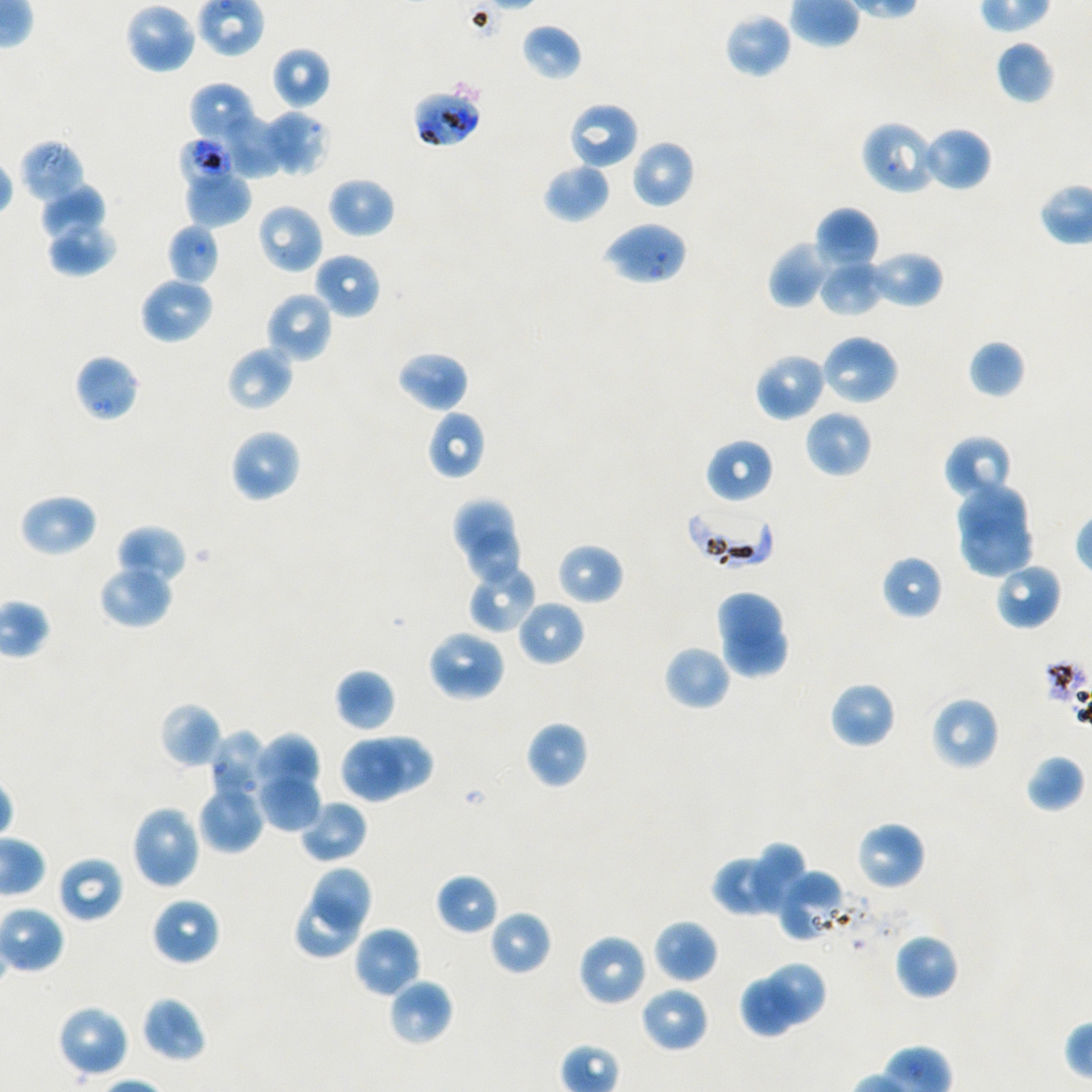

Not every red blood cell is marked. A life-cycle stage — or a range of stages, where the recorded stages span more than one — follows each staged infected red blood cell.
locations of uninfected red blood cells = approximate bounding rectangles given as corner coordinates in pixels from the top-left: (x1=124, y1=2, x2=197, y2=74), (x1=723, y1=12, x2=793, y2=78), (x1=521, y1=23, x2=583, y2=81), (x1=995, y1=40, x2=1055, y2=105), (x1=270, y1=46, x2=331, y2=110), (x1=189, y1=83, x2=260, y2=145), (x1=566, y1=101, x2=640, y2=170), (x1=261, y1=111, x2=331, y2=176), (x1=220, y1=117, x2=285, y2=179), (x1=921, y1=126, x2=992, y2=192), (x1=632, y1=140, x2=695, y2=209), (x1=543, y1=162, x2=611, y2=223), (x1=184, y1=167, x2=251, y2=226), (x1=327, y1=176, x2=396, y2=238), (x1=39, y1=185, x2=107, y2=240), (x1=256, y1=204, x2=323, y2=275), (x1=816, y1=206, x2=879, y2=271), (x1=46, y1=219, x2=116, y2=277), (x1=768, y1=240, x2=833, y2=308), (x1=867, y1=250, x2=944, y2=310), (x1=313, y1=252, x2=381, y2=319), (x1=819, y1=261, x2=885, y2=316), (x1=138, y1=276, x2=214, y2=344), (x1=265, y1=291, x2=334, y2=363), (x1=819, y1=333, x2=900, y2=407), (x1=968, y1=340, x2=1026, y2=399), (x1=225, y1=346, x2=294, y2=412), (x1=396, y1=350, x2=469, y2=413), (x1=754, y1=351, x2=826, y2=422), (x1=74, y1=354, x2=140, y2=422), (x1=426, y1=409, x2=486, y2=480), (x1=805, y1=410, x2=873, y2=478), (x1=229, y1=428, x2=302, y2=503), (x1=943, y1=434, x2=1015, y2=503), (x1=705, y1=437, x2=774, y2=505), (x1=958, y1=483, x2=1025, y2=546), (x1=19, y1=493, x2=98, y2=558), (x1=456, y1=500, x2=514, y2=556), (x1=962, y1=520, x2=1032, y2=577), (x1=115, y1=525, x2=187, y2=589), (x1=469, y1=531, x2=522, y2=581), (x1=556, y1=543, x2=624, y2=605), (x1=881, y1=555, x2=943, y2=619), (x1=994, y1=561, x2=1062, y2=631), (x1=467, y1=562, x2=539, y2=634), (x1=98, y1=564, x2=174, y2=630), (x1=718, y1=589, x2=781, y2=645), (x1=517, y1=599, x2=585, y2=667), (x1=722, y1=623, x2=786, y2=676), (x1=426, y1=629, x2=507, y2=702), (x1=663, y1=644, x2=731, y2=711), (x1=334, y1=668, x2=396, y2=733), (x1=829, y1=680, x2=896, y2=750), (x1=930, y1=696, x2=1000, y2=771), (x1=159, y1=702, x2=223, y2=769), (x1=525, y1=721, x2=589, y2=788), (x1=208, y1=731, x2=269, y2=805), (x1=254, y1=733, x2=321, y2=793), (x1=371, y1=734, x2=433, y2=793), (x1=344, y1=740, x2=401, y2=801), (x1=1025, y1=753, x2=1085, y2=813), (x1=254, y1=769, x2=322, y2=832), (x1=198, y1=782, x2=265, y2=854), (x1=299, y1=799, x2=368, y2=864), (x1=130, y1=804, x2=202, y2=891), (x1=855, y1=820, x2=926, y2=891), (x1=746, y1=842, x2=806, y2=911), (x1=710, y1=848, x2=798, y2=917), (x1=56, y1=854, x2=124, y2=924), (x1=312, y1=867, x2=371, y2=930), (x1=774, y1=868, x2=849, y2=943), (x1=436, y1=873, x2=499, y2=935), (x1=151, y1=896, x2=221, y2=966), (x1=297, y1=896, x2=358, y2=958), (x1=488, y1=909, x2=551, y2=976), (x1=653, y1=919, x2=718, y2=984), (x1=352, y1=926, x2=421, y2=998), (x1=894, y1=932, x2=960, y2=1000), (x1=577, y1=933, x2=649, y2=1007), (x1=769, y1=964, x2=825, y2=1023), (x1=387, y1=978, x2=452, y2=1047), (x1=739, y1=981, x2=798, y2=1038), (x1=639, y1=985, x2=710, y2=1054), (x1=140, y1=996, x2=207, y2=1063), (x1=55, y1=1004, x2=130, y2=1079)
objective = 100x, oil immersion, numerical aperture 1.45
culture = static in-vitro P. falciparum strain NF54
locations of infected red blood cells = approximate bounding rectangles given as corner coordinates in pixels from the top-left: (x1=413, y1=88, x2=483, y2=148) late trophozoite; (x1=684, y1=502, x2=775, y2=569)
stain = Giemsa
locations of red blood cells of indeterminate infection status = approximate bounding rectangles given as corner coordinates in pixels from the top-left: (x1=860, y1=120, x2=939, y2=196), (x1=176, y1=136, x2=237, y2=196), (x1=18, y1=139, x2=86, y2=203), (x1=602, y1=221, x2=689, y2=286), (x1=166, y1=223, x2=221, y2=287)
preparation = thin blood film
donor blood group = A+/O+
field of view = single
image size = 1092×1092 pixels